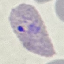
Result: malaria parasites detected. Automatically extracted cell patch, resized to 64 × 64 pixels. Giemsa stain. Thin blood smear. Photographed with a smartphone camera at the microscope eyepiece.